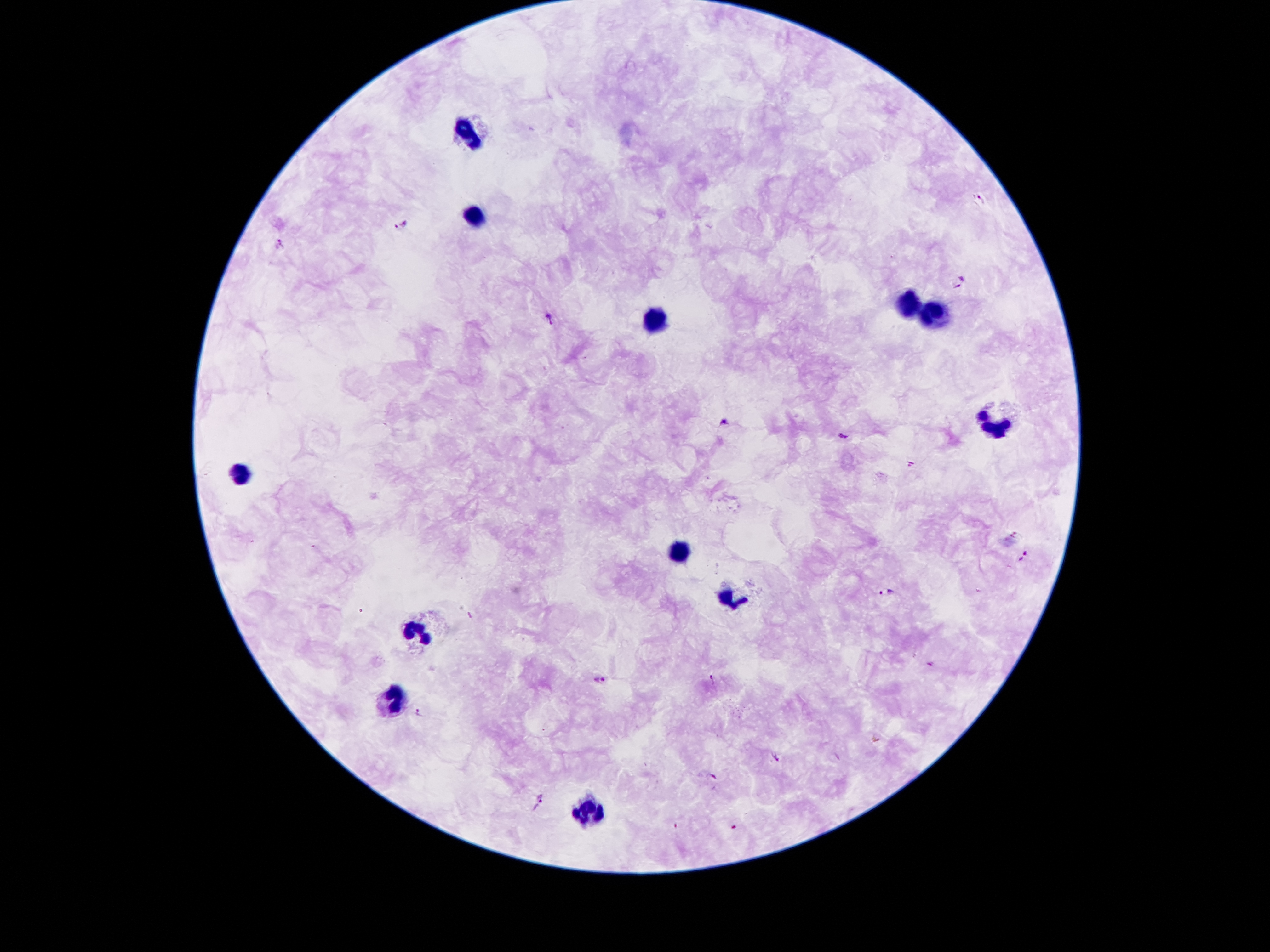
coordinate format = approximate centers as {x, y} in pixels
malaria parasite locations = {981, 199}, {404, 226}, {279, 245}, {958, 283}, {549, 319}, {724, 421}, {842, 438}, {911, 464}, {1024, 556}, {888, 591}, {600, 679}, {712, 680}, {420, 711}, {776, 756}, {710, 779}, {540, 801}, {734, 828}
leukocyte locations = {466, 129}, {470, 218}, {909, 304}, {938, 316}, {657, 323}, {996, 422}, {237, 478}, {676, 555}, {731, 593}, {418, 630}, {395, 698}, {589, 813}
magnification = 100x
image size = 1270×952 pixels
stain = Giemsa
field of view = single
preparation = thick blood smear
capture = smartphone camera through the microscope eyepiece
patient malaria status = positive for Plasmodium falciparum